Classify this cell by malaria status.
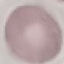
Uninfected.

Summary:
  - Preparation: thin blood film
  - Stain: Giemsa
  - Image type: automatically extracted cell patch, resized to 64 × 64 pixels
  - Capture: smartphone through the microscope eyepiece